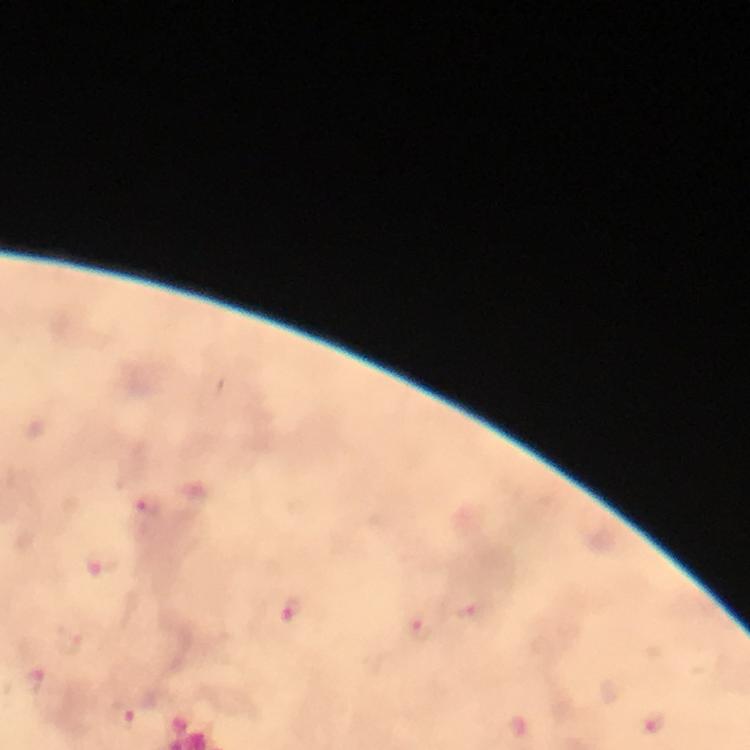

Approximate centers as {x, y} in pixels.
Summary:
  - Plasmodium parasite locations: {147, 507}, {102, 564}, {291, 609}, {470, 611}, {419, 626}, {30, 680}, {120, 716}, {651, 723}
  - Preparation: thick blood film
  - Magnification: 100x
  - Immersion oil: used
  - Capture: smartphone camera through the microscope
  - Image size: 750×750 pixels
  - Stain: Giemsa
  - Context: from a diagnostic examination for malaria
  - Cropped from: a single field of view